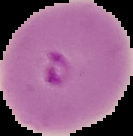 From a thin blood film. Segmented cell region on a black background. Image is 133×136 pixels. Result: Plasmodium parasites identified.